Assess for malaria.
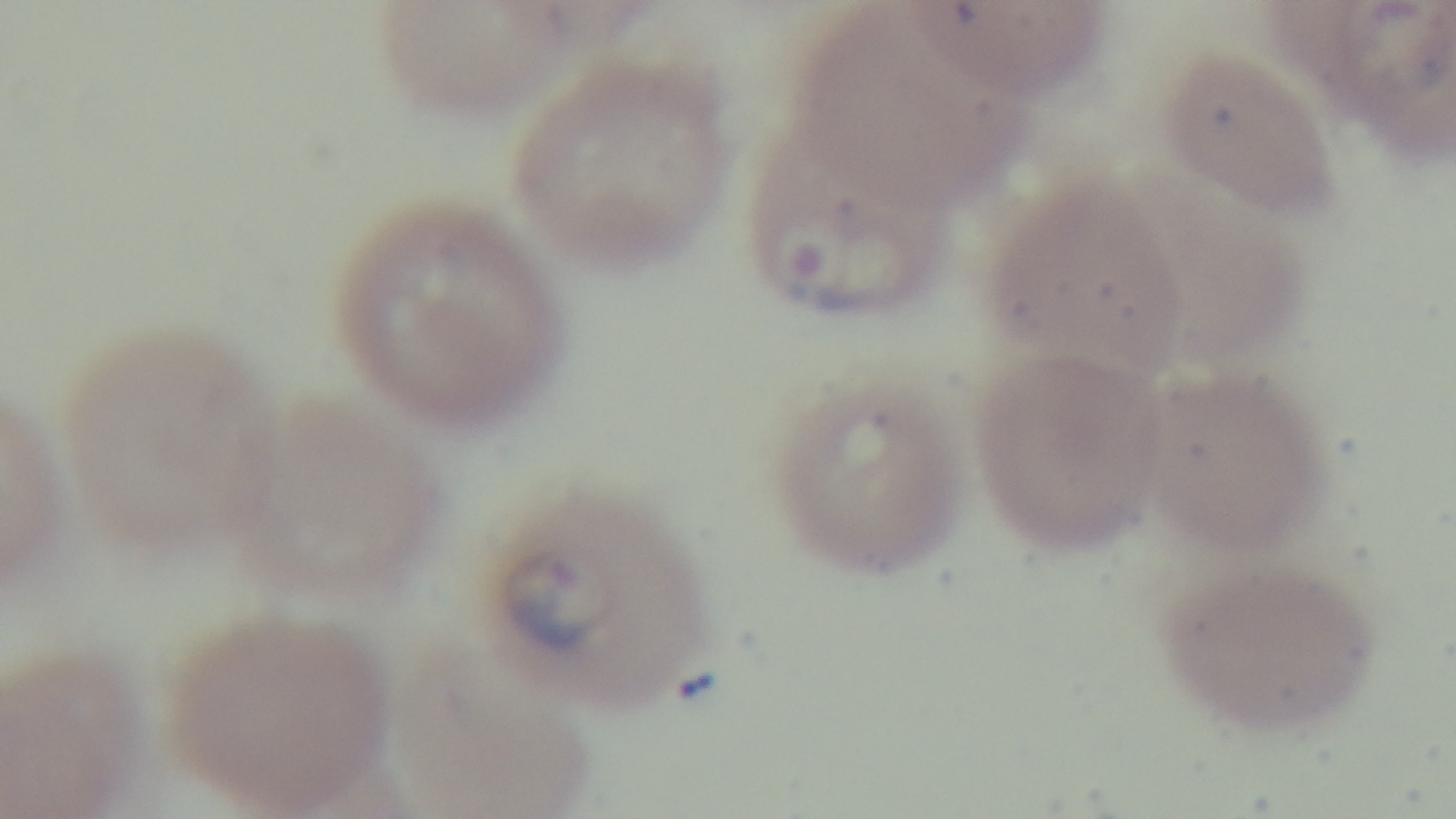

Infected.

Summary:
  - Stain: Giemsa
  - Objective: 100x oil immersion
  - Capture: mounted 4K digital camera
  - Preparation: thin blood film
  - Field of view: single
  - Modality: light microscopy